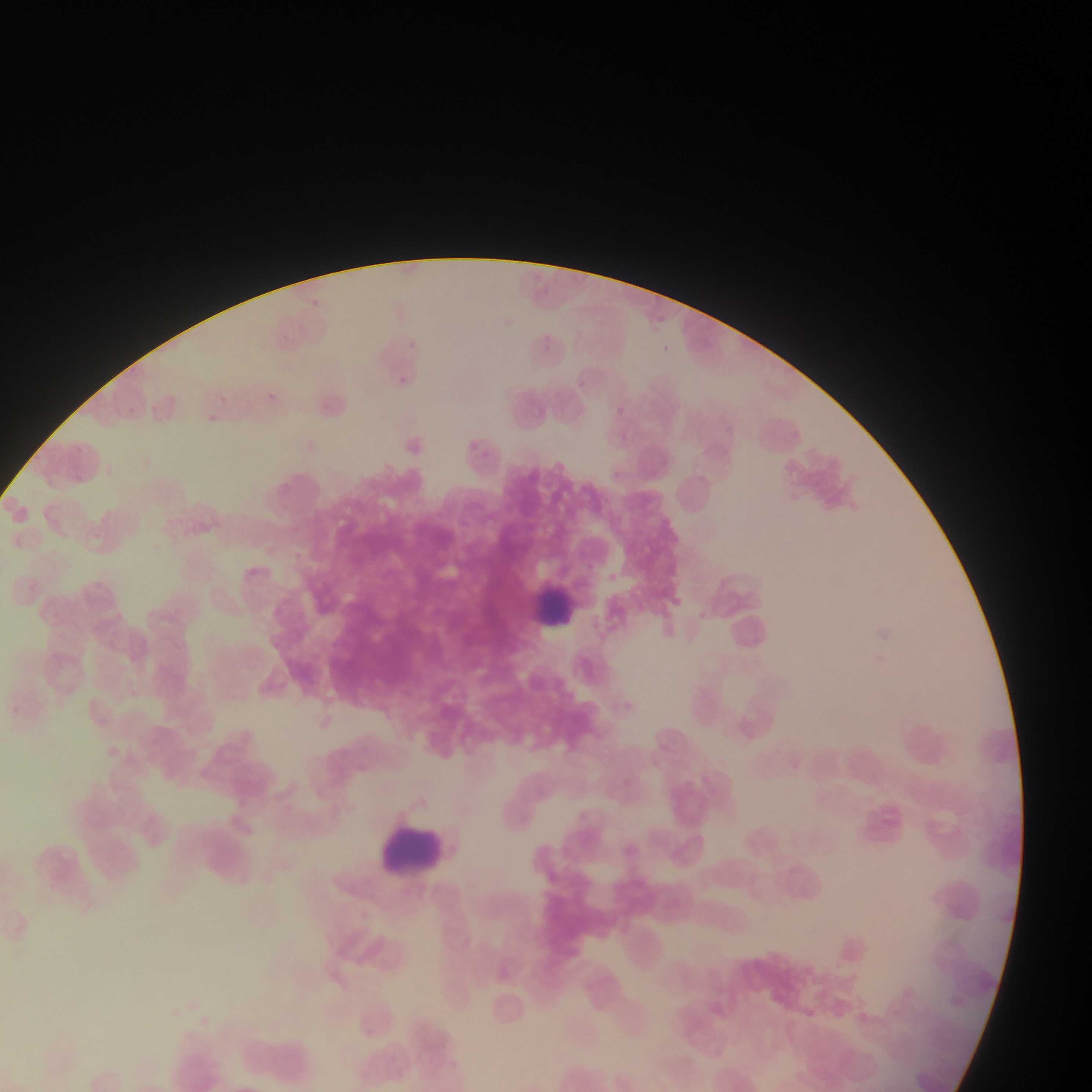

Approximate bounding boxes as {left, top, right, bottom} in pixels. Leukocyte locations: {530, 575, 603, 633}, {382, 816, 447, 879}. Collected in Ghana. Mobile-phone photograph taken through the microscope. Image is 1092×1092 pixels. One field of view. Thin blood film.